Comment on the morphology of the red blood cells.
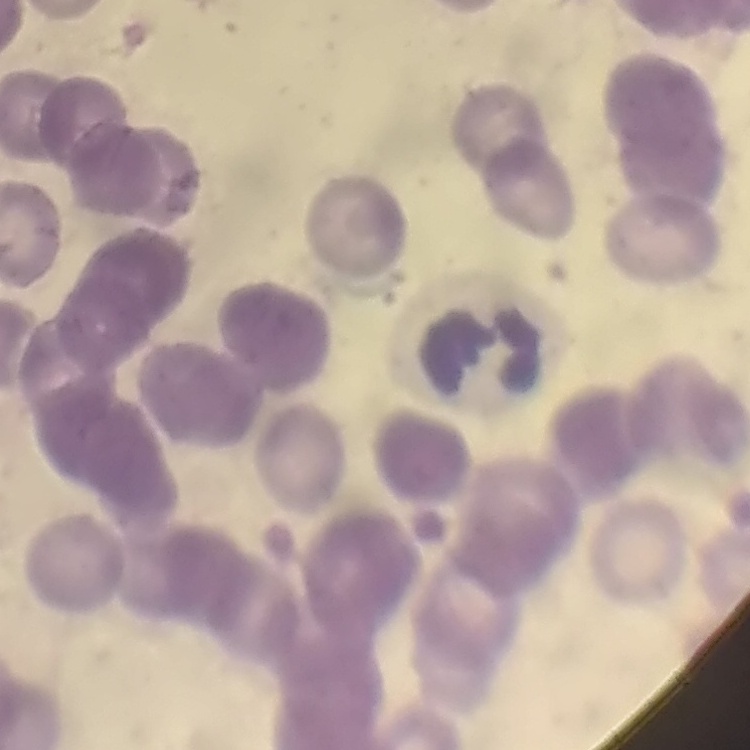
Rouleaux formation.

Square crop of a larger photomicrograph. Field's or Giemsa stain. Thin peripheral smear.